Comment on the morphology of the red blood cells.
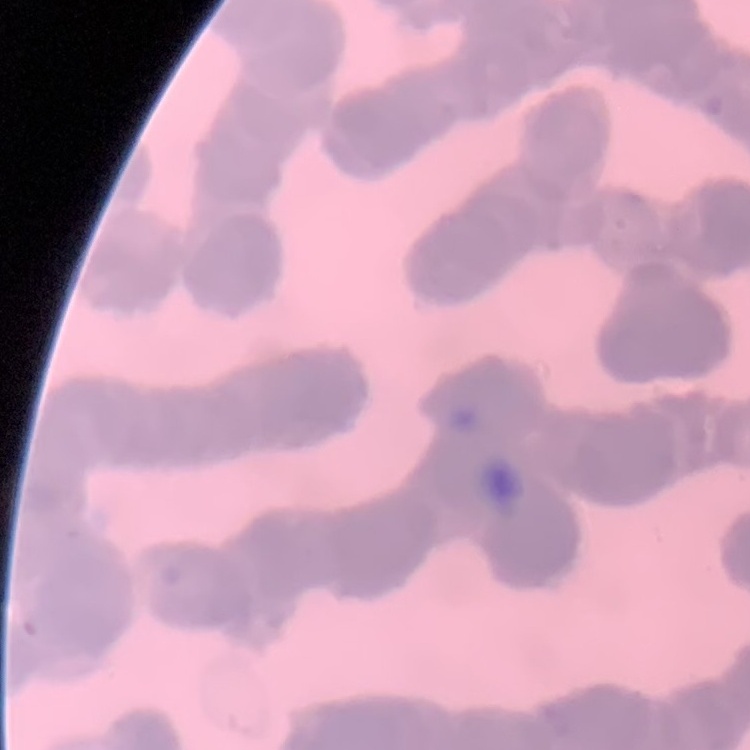

They show rouleaux formation.

Thin blood smear. Square crop of a larger photomicrograph. Stained with either Field's or Giemsa.